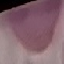
Summary:
  - Malaria status: uninfected
  - Capture: smartphone camera at the microscope eyepiece
  - Stain: Giemsa
  - Preparation: thin blood smear
  - Image type: cell patch, automatically extracted from a larger field of view and resized to 64 × 64 pixels